Assess this cell for malaria.
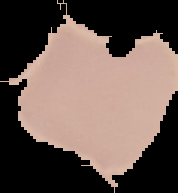

Uninfected.

Summary:
  - Image type: cell region segmented out of the field of view; surrounding area masked to black
  - Preparation: thin blood smear
  - Image size: 178×193 pixels